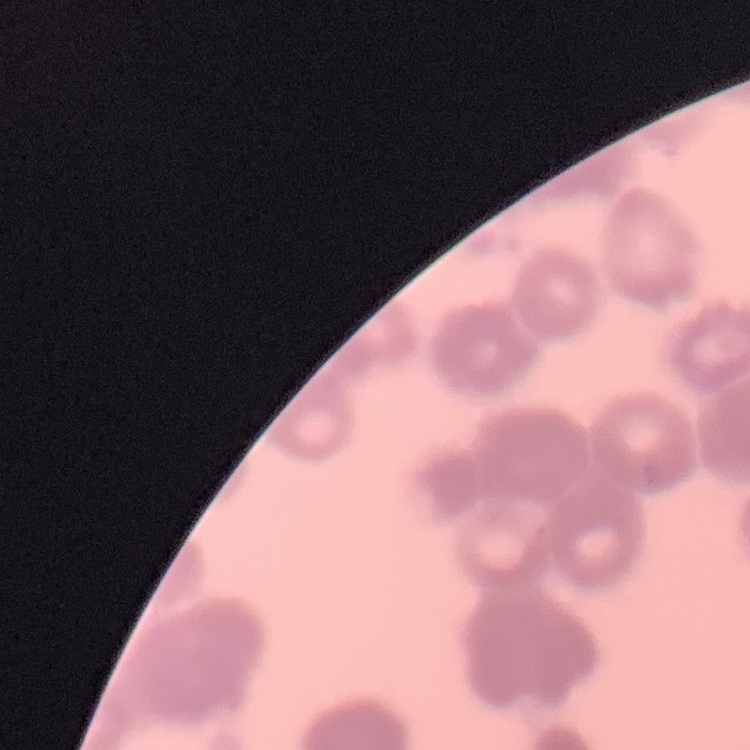

Summary:
  - Erythrocyte morphology: rouleaux formation
  - Stain: Field's or Giemsa
  - Preparation: thin blood smear
  - Image type: one tile cut from a larger photomicrograph